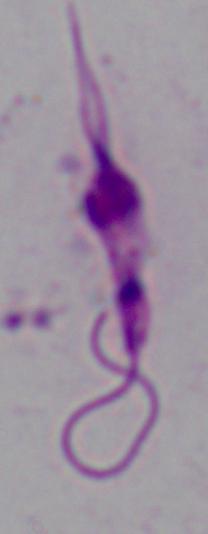

A Leishmania parasite is seen. 1000x magnification. Micrograph.